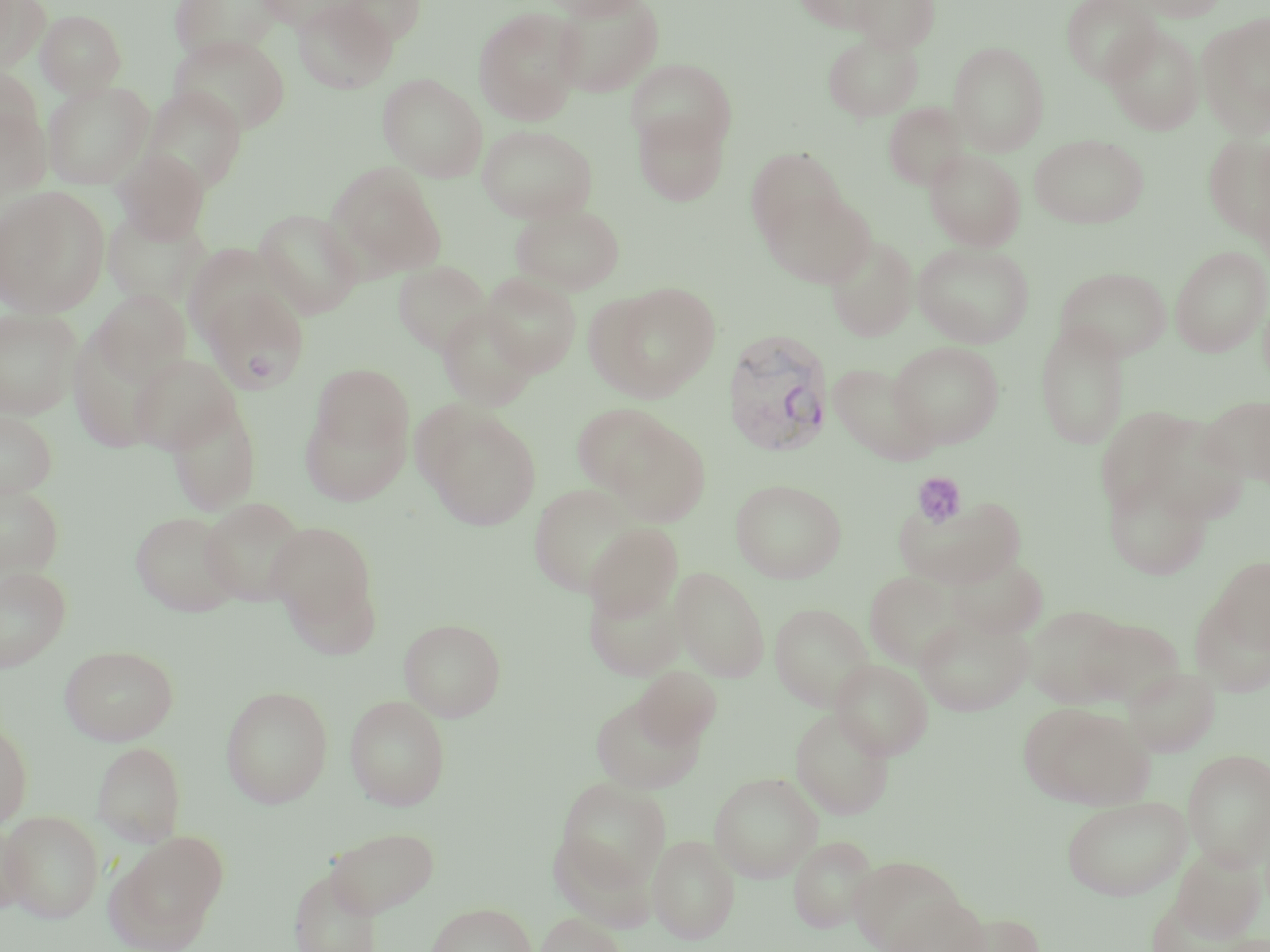

Summary:
  - Coordinate format: approximate bounding boxes as named x1/y1/x2/y2 corners in pixels
  - Uninfected red blood cell locations: (x1=0, y1=0, x2=50, y2=72), (x1=169, y1=0, x2=283, y2=62), (x1=256, y1=0, x2=362, y2=33), (x1=292, y1=0, x2=396, y2=94), (x1=337, y1=0, x2=427, y2=46), (x1=541, y1=0, x2=650, y2=19), (x1=792, y1=0, x2=895, y2=34), (x1=848, y1=0, x2=941, y2=53), (x1=1060, y1=0, x2=1162, y2=85), (x1=1130, y1=0, x2=1230, y2=22), (x1=551, y1=1, x2=665, y2=98), (x1=472, y1=6, x2=585, y2=126), (x1=35, y1=9, x2=127, y2=98), (x1=1198, y1=13, x2=1270, y2=139), (x1=1104, y1=24, x2=1204, y2=135), (x1=823, y1=32, x2=923, y2=122), (x1=169, y1=34, x2=291, y2=136), (x1=948, y1=41, x2=1049, y2=155), (x1=625, y1=58, x2=737, y2=155), (x1=0, y1=63, x2=45, y2=158), (x1=378, y1=73, x2=488, y2=182), (x1=42, y1=80, x2=154, y2=189), (x1=141, y1=86, x2=248, y2=193), (x1=0, y1=98, x2=52, y2=200), (x1=882, y1=101, x2=970, y2=190), (x1=632, y1=108, x2=731, y2=207), (x1=477, y1=124, x2=597, y2=223), (x1=1030, y1=133, x2=1149, y2=229), (x1=1203, y1=133, x2=1270, y2=243), (x1=745, y1=147, x2=847, y2=245), (x1=113, y1=149, x2=210, y2=244), (x1=924, y1=149, x2=1026, y2=250), (x1=328, y1=163, x2=447, y2=277), (x1=0, y1=187, x2=110, y2=317), (x1=761, y1=188, x2=876, y2=286), (x1=510, y1=203, x2=626, y2=295), (x1=102, y1=208, x2=213, y2=309), (x1=254, y1=208, x2=363, y2=319), (x1=825, y1=236, x2=919, y2=341), (x1=913, y1=241, x2=1035, y2=347), (x1=1170, y1=245, x2=1270, y2=357), (x1=392, y1=260, x2=492, y2=356), (x1=1054, y1=266, x2=1172, y2=362), (x1=481, y1=273, x2=582, y2=376), (x1=594, y1=281, x2=722, y2=401), (x1=200, y1=284, x2=309, y2=393), (x1=93, y1=290, x2=191, y2=386), (x1=437, y1=306, x2=539, y2=411), (x1=0, y1=308, x2=83, y2=419), (x1=1035, y1=320, x2=1131, y2=450), (x1=888, y1=341, x2=1005, y2=448), (x1=128, y1=354, x2=240, y2=454), (x1=828, y1=362, x2=941, y2=465), (x1=312, y1=363, x2=413, y2=456), (x1=1201, y1=396, x2=1270, y2=486), (x1=165, y1=397, x2=262, y2=516), (x1=299, y1=402, x2=411, y2=506), (x1=571, y1=402, x2=675, y2=496), (x1=417, y1=404, x2=542, y2=530), (x1=1093, y1=405, x2=1200, y2=519), (x1=0, y1=410, x2=58, y2=499), (x1=1133, y1=411, x2=1250, y2=526), (x1=604, y1=417, x2=712, y2=526), (x1=1104, y1=471, x2=1213, y2=580), (x1=731, y1=479, x2=847, y2=583), (x1=0, y1=482, x2=64, y2=579), (x1=529, y1=484, x2=642, y2=595), (x1=895, y1=494, x2=1026, y2=589), (x1=199, y1=497, x2=309, y2=606), (x1=131, y1=511, x2=241, y2=617), (x1=266, y1=521, x2=379, y2=642), (x1=584, y1=523, x2=682, y2=623), (x1=947, y1=553, x2=1048, y2=639), (x1=1213, y1=556, x2=1270, y2=654), (x1=0, y1=566, x2=71, y2=671), (x1=672, y1=567, x2=770, y2=681), (x1=864, y1=570, x2=965, y2=669), (x1=584, y1=579, x2=686, y2=681), (x1=1189, y1=597, x2=1270, y2=698), (x1=769, y1=603, x2=875, y2=711), (x1=1023, y1=604, x2=1131, y2=708), (x1=914, y1=613, x2=1034, y2=716), (x1=1075, y1=615, x2=1184, y2=707), (x1=398, y1=617, x2=507, y2=721), (x1=60, y1=644, x2=178, y2=745), (x1=831, y1=659, x2=933, y2=759), (x1=1122, y1=664, x2=1220, y2=756), (x1=632, y1=665, x2=722, y2=750), (x1=220, y1=685, x2=333, y2=808), (x1=344, y1=695, x2=450, y2=810), (x1=590, y1=695, x2=705, y2=793), (x1=1020, y1=701, x2=1153, y2=810), (x1=790, y1=707, x2=894, y2=819), (x1=0, y1=717, x2=32, y2=829), (x1=92, y1=741, x2=187, y2=847), (x1=1182, y1=749, x2=1270, y2=870), (x1=709, y1=771, x2=823, y2=882), (x1=556, y1=777, x2=671, y2=891), (x1=1061, y1=795, x2=1191, y2=901), (x1=1, y1=810, x2=105, y2=923), (x1=0, y1=821, x2=28, y2=919), (x1=326, y1=826, x2=439, y2=918), (x1=107, y1=831, x2=229, y2=950), (x1=549, y1=832, x2=656, y2=932), (x1=648, y1=834, x2=739, y2=943), (x1=789, y1=835, x2=879, y2=933), (x1=1167, y1=844, x2=1267, y2=945), (x1=848, y1=855, x2=969, y2=952), (x1=289, y1=867, x2=383, y2=952), (x1=882, y1=891, x2=991, y2=952), (x1=426, y1=902, x2=536, y2=952), (x1=946, y1=910, x2=1046, y2=952), (x1=535, y1=912, x2=626, y2=952)
  - Platelet locations: (x1=911, y1=472, x2=968, y2=528)
  - Plasmodium vivax-infected red blood cell locations: (x1=721, y1=329, x2=836, y2=457)
  - Slide-level diagnosis: Plasmodium vivax
  - Field of view: one of a larger specimen
  - Image size: 1270×952 pixels
  - Stain: May-Grünwald-Giemsa
  - Preparation: thin blood smear
  - Modality: optical microscopy
  - Magnification: 1000x